State which parasite is depicted.
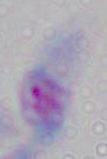
This is Toxoplasma gondii.

1000x magnification. Micrograph.